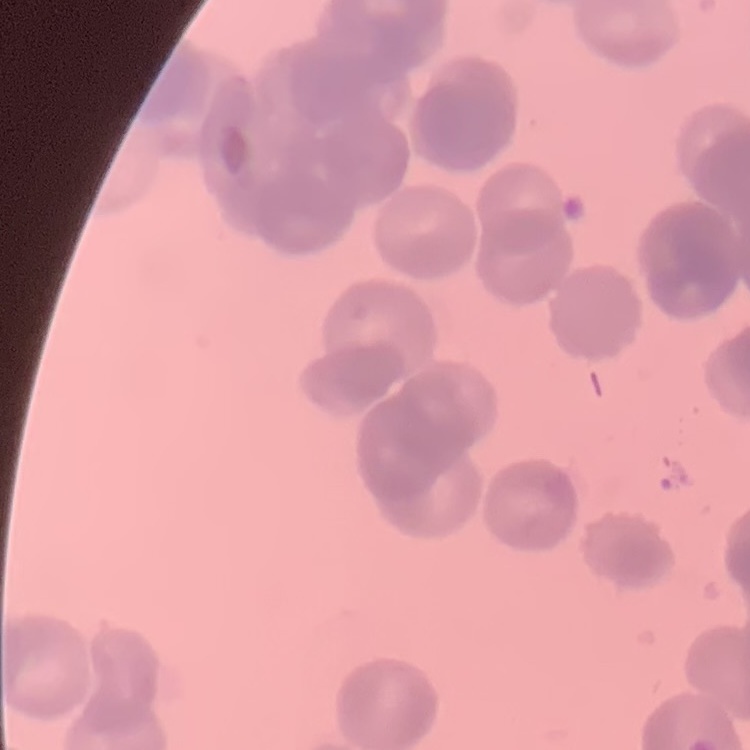
Summary:
  - Erythrocyte morphology: rouleaux formation
  - Stain: Field's or Giemsa
  - Image type: square crop of a larger photomicrograph
  - Preparation: thin blood film